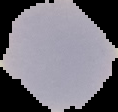

image type = cell region segmented out of the field of view; surrounding area masked to black
preparation = thin blood smear
image size = 118×112 pixels
malaria status = uninfected